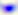

magnification: 400x
identification: Toxoplasma gondii
modality: micrograph